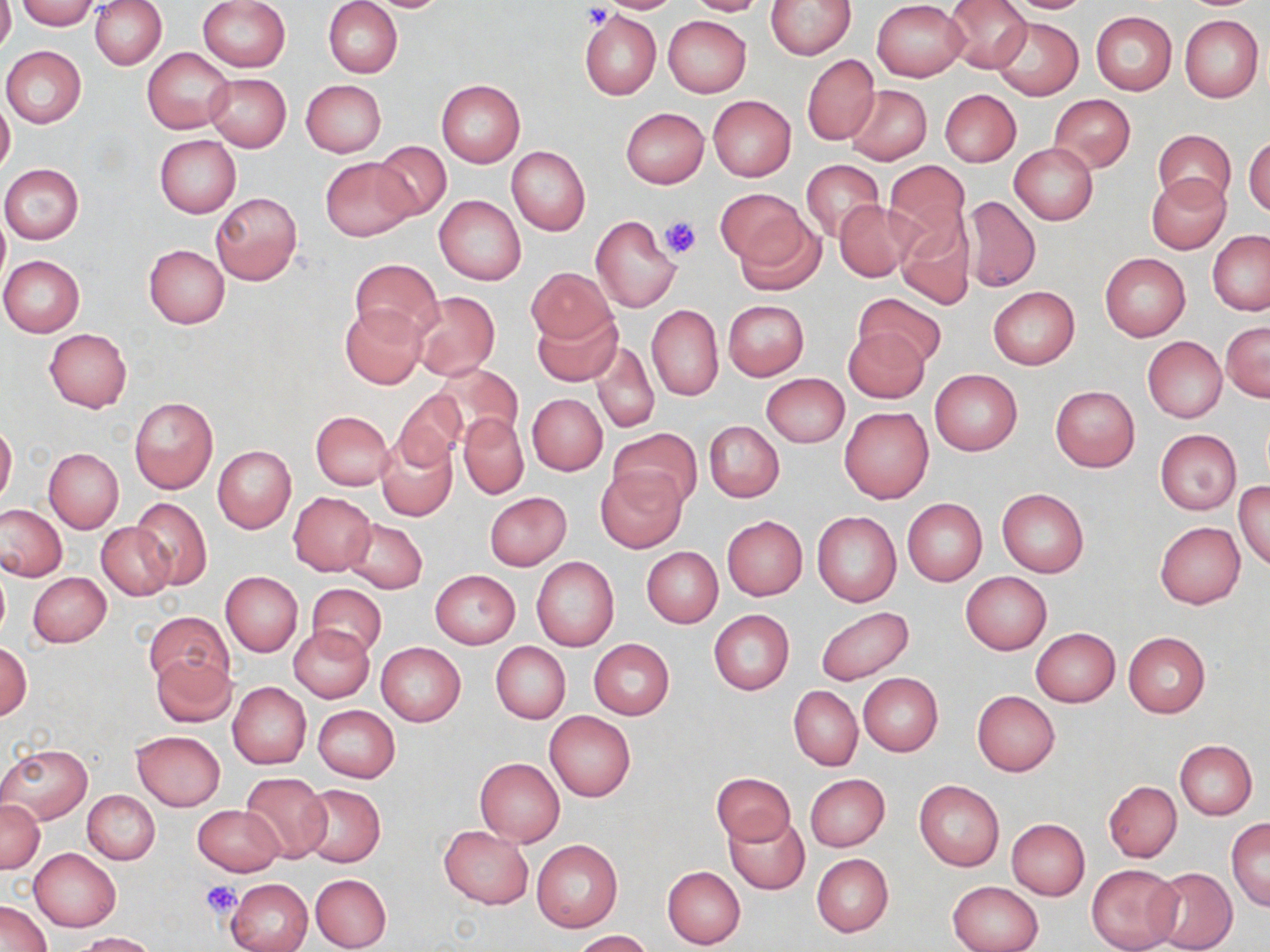

slide-level diagnosis = no evidence of blood parasites
uninfected red blood cell locations = approximate bounding boxes as (x1,y1)-(x2,y2) corner pairs in pixels: (0,0)-(15,53), (17,0)-(99,30), (197,0)-(289,72), (323,0)-(402,78), (595,0)-(681,14), (685,0)-(767,16), (766,0)-(856,59), (945,0)-(1030,73), (998,0)-(1095,13), (91,1)-(167,69), (362,1)-(454,12), (873,1)-(968,81), (579,9)-(662,101), (1090,11)-(1177,95), (663,15)-(752,97), (1179,15)-(1264,103), (990,17)-(1084,101), (1,46)-(86,128), (143,47)-(233,134), (802,54)-(881,145), (205,74)-(291,152), (301,79)-(386,157), (435,80)-(525,167), (845,84)-(932,164), (941,90)-(1021,166), (1048,94)-(1135,172), (708,95)-(795,181), (0,100)-(14,177), (622,108)-(708,188), (1154,129)-(1235,208), (1245,134)-(1270,218), (154,135)-(241,218), (372,141)-(453,221), (1009,144)-(1098,225), (507,146)-(590,236), (320,158)-(415,241), (800,159)-(884,240), (883,159)-(970,248), (1,164)-(84,244), (1146,173)-(1231,255), (716,188)-(807,265), (845,190)-(971,288), (211,193)-(301,284), (435,195)-(525,285), (962,195)-(1040,291), (834,201)-(913,281), (0,213)-(9,288), (735,213)-(825,295), (591,215)-(680,312), (897,218)-(976,310), (1208,232)-(1270,315), (144,245)-(229,329), (1100,253)-(1191,341), (0,255)-(86,337), (350,259)-(441,339), (527,267)-(614,344), (988,286)-(1079,369), (410,291)-(500,381), (855,293)-(946,369), (723,300)-(808,380), (647,304)-(724,400), (340,305)-(428,389), (532,308)-(621,387), (1222,322)-(1269,402), (843,327)-(930,403), (44,328)-(132,412), (1143,337)-(1226,422), (591,340)-(660,434), (432,362)-(524,446), (929,369)-(1022,456), (761,373)-(849,447), (1050,385)-(1140,471), (392,390)-(466,470), (528,393)-(607,474), (129,397)-(218,493), (839,407)-(934,503), (311,410)-(394,491), (458,414)-(528,498), (704,420)-(784,502), (0,421)-(16,505), (608,427)-(702,511), (1154,429)-(1243,515), (377,434)-(456,520), (213,446)-(296,533), (45,448)-(124,533), (595,466)-(687,554), (1235,480)-(1270,571), (996,488)-(1089,577), (484,492)-(570,570), (287,493)-(375,575), (129,496)-(212,591), (902,499)-(987,585), (0,504)-(66,581), (812,511)-(901,607), (722,515)-(807,600), (344,518)-(427,594), (1156,522)-(1245,608), (97,524)-(175,600), (642,546)-(723,628), (531,557)-(618,652), (0,563)-(10,642), (430,569)-(520,650), (27,572)-(111,647), (220,572)-(303,657), (960,572)-(1051,654), (307,583)-(387,659), (815,606)-(915,686), (708,610)-(793,696), (144,611)-(232,692), (288,624)-(374,702), (1031,628)-(1120,706), (1122,631)-(1211,717), (588,639)-(674,720), (0,642)-(31,721), (491,642)-(571,724), (375,643)-(465,727), (151,654)-(236,727), (857,672)-(944,756), (228,682)-(311,769), (788,686)-(863,769), (972,690)-(1060,777), (313,705)-(400,782), (546,711)-(636,801), (131,730)-(225,811), (1175,741)-(1256,820), (0,742)-(91,824), (474,758)-(565,847), (711,771)-(795,846), (240,772)-(331,863), (804,774)-(889,852), (914,781)-(1004,872), (1103,781)-(1182,862), (301,784)-(386,866), (83,791)-(160,865), (0,799)-(44,872), (193,804)-(286,877), (725,816)-(809,894), (1227,817)-(1270,910), (1006,818)-(1089,900), (438,825)-(534,909), (532,840)-(622,932), (30,849)-(121,930), (813,853)-(894,937), (1086,863)-(1182,952), (662,866)-(745,948), (1150,866)-(1236,952), (310,873)-(392,951), (227,877)-(314,952), (948,880)-(1042,952), (1,899)-(52,952), (574,930)-(651,951), (75,932)-(158,952)
magnification = 1000x
image size = 1270×952 pixels
preparation = thin blood film
modality = light microscopy
stain = May-Grünwald-Giemsa
field of view = one of a larger specimen
platelet locations = approximate bounding boxes as (x1,y1)-(x2,y2) corner pairs in pixels: (580,3)-(613,28), (658,214)-(701,259), (201,880)-(242,919)